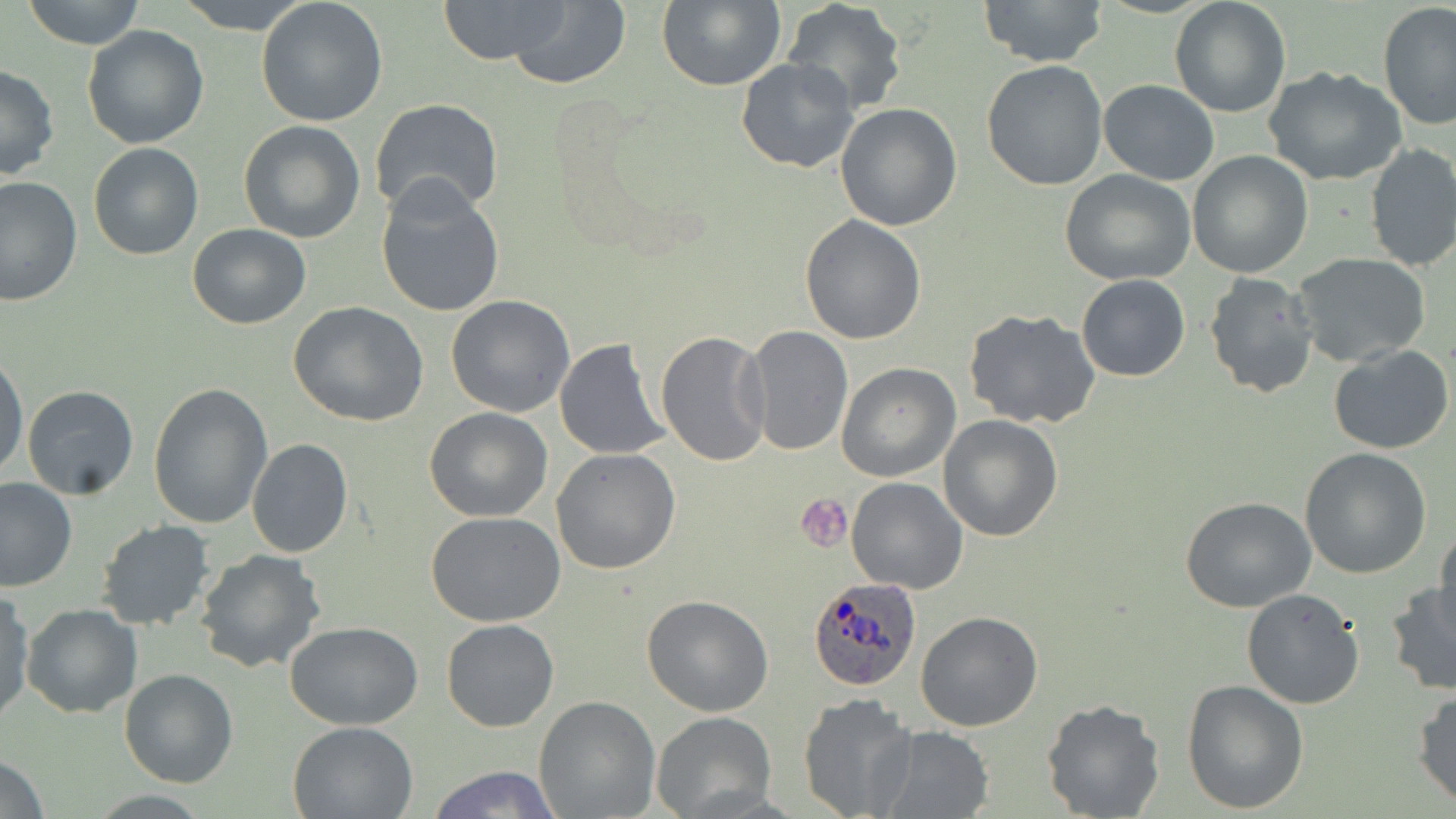

Approximate bounding boxes as [x1, y1, x2, y2] in pixels. Plasmodium ovale-infected red blood cell locations: [808, 578, 921, 691]. Platelet locations: [797, 494, 853, 552]. Uninfected red blood cell locations: [22, 0, 146, 50], [174, 0, 313, 34], [255, 0, 389, 126], [435, 0, 574, 64], [506, 0, 632, 89], [656, 0, 785, 90], [980, 0, 1107, 68], [1169, 0, 1291, 117], [782, 2, 908, 114], [1377, 4, 1456, 130], [81, 25, 210, 149], [735, 56, 859, 173], [981, 60, 1107, 190], [0, 65, 60, 180], [1264, 67, 1408, 186], [1099, 79, 1219, 184], [369, 99, 505, 222], [833, 103, 962, 231], [238, 120, 366, 243], [88, 142, 203, 260], [1364, 143, 1456, 272], [1187, 151, 1314, 278], [1059, 168, 1197, 285], [0, 176, 82, 306], [376, 178, 506, 319], [799, 215, 927, 343], [187, 223, 311, 330], [1294, 254, 1432, 368], [1203, 272, 1320, 398], [1076, 274, 1190, 382], [445, 294, 576, 417], [288, 302, 430, 426], [962, 308, 1101, 429], [742, 326, 854, 456], [656, 330, 773, 468], [554, 337, 671, 461], [1329, 345, 1453, 455], [0, 351, 28, 483], [836, 362, 960, 481], [148, 382, 274, 529], [22, 384, 140, 499], [425, 406, 552, 523], [938, 414, 1065, 540], [246, 438, 352, 557], [1300, 447, 1432, 578], [550, 449, 680, 575], [845, 476, 967, 593], [0, 477, 76, 592], [1180, 495, 1318, 612], [426, 512, 568, 626], [97, 520, 216, 631], [1433, 527, 1456, 631], [194, 548, 329, 676], [1386, 581, 1456, 695], [1241, 588, 1365, 711], [0, 589, 34, 724], [642, 595, 774, 716], [21, 603, 142, 717], [914, 610, 1043, 731], [442, 618, 559, 731], [285, 619, 424, 730], [119, 668, 237, 788], [1181, 679, 1309, 813], [1412, 689, 1456, 808], [798, 692, 917, 819], [534, 696, 660, 818], [1041, 699, 1165, 819], [652, 711, 776, 819], [288, 719, 419, 818], [872, 726, 994, 818], [0, 753, 49, 818], [424, 764, 563, 819]. Slide-level diagnosis: Plasmodium ovale. Image is 1456×819 pixels. Light microscopy. May-Grünwald-Giemsa-stained preparation. Captured at 1000x magnification. One field of a larger specimen. Thin blood smear.